Outline each blood parasite and name the species.
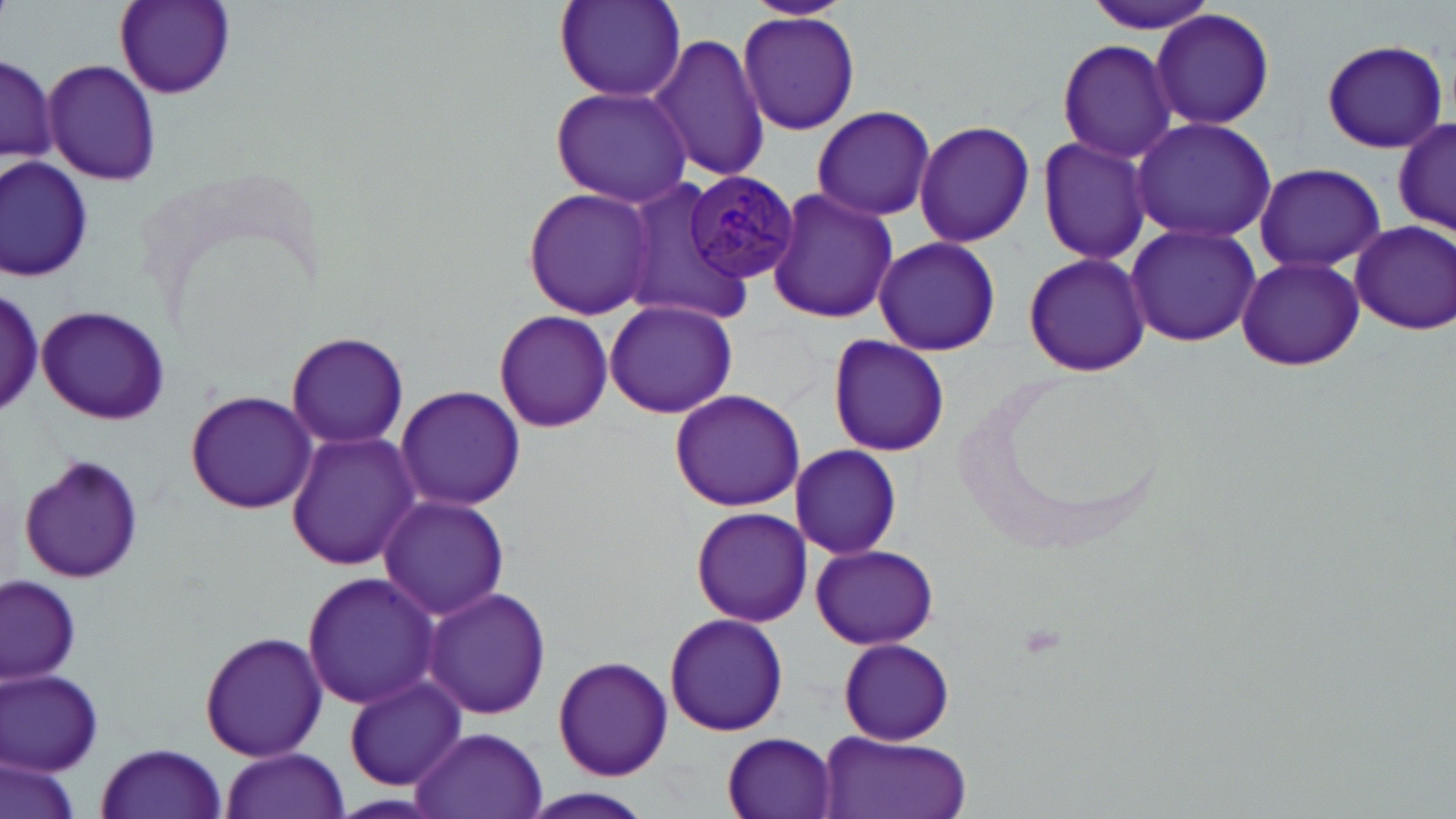

Approximate bounding boxes as (x1,y1)-(x2,y2) corner pairs in pixels.
Plasmodium malariae-infected red blood cells: (684,171)-(798,285).
No Plasmodium falciparum, Plasmodium ovale, Plasmodium vivax, Babesia divergens, or Trypanosoma brucei observed.

slide-level diagnosis = Plasmodium malariae
uninfected red blood cell locations = approximate bounding boxes as (x1,y1)-(x2,y2) corner pairs in pixels: (114,0)-(235,99), (552,0)-(686,104), (738,0)-(854,21), (1080,1)-(1223,35), (1150,8)-(1276,133), (737,10)-(860,134), (651,32)-(767,185), (1321,38)-(1448,154), (1056,39)-(1177,162), (1,52)-(56,170), (42,58)-(160,188), (552,85)-(695,207), (810,106)-(937,222), (1391,112)-(1453,242), (1130,117)-(1279,244), (913,119)-(1035,248), (1036,134)-(1154,267), (1,159)-(93,281), (1254,162)-(1385,273), (619,178)-(756,326), (523,187)-(659,321), (765,187)-(899,324), (1349,219)-(1455,336), (1125,222)-(1258,347), (872,237)-(1001,356), (1024,250)-(1150,378), (1234,253)-(1365,373), (0,287)-(46,423), (605,300)-(739,416), (36,303)-(172,426), (493,310)-(613,432), (287,331)-(409,449), (828,335)-(951,459), (957,369)-(1175,556), (396,384)-(525,511), (184,388)-(317,515), (668,389)-(807,512), (285,430)-(419,570), (789,444)-(903,558), (15,454)-(146,588), (378,494)-(511,620), (689,507)-(810,626), (810,544)-(940,651), (301,570)-(442,709), (1,575)-(80,684), (423,586)-(549,721), (664,611)-(789,737), (198,631)-(329,762), (839,637)-(955,745), (553,655)-(671,780), (1,670)-(104,773), (343,675)-(466,789), (409,726)-(550,819), (816,729)-(971,819), (722,733)-(838,817), (94,743)-(229,818), (218,747)-(349,819), (1,756)-(80,819), (517,788)-(660,819)
modality = optical microscopy
field of view = one of a larger specimen
image size = 1456×819 pixels
preparation = thin blood smear
magnification = 1000x
stain = May-Grünwald-Giemsa